Identify the parasite.
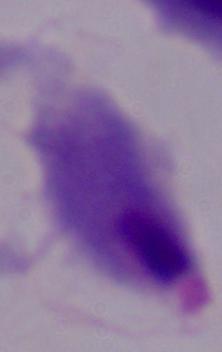
This is a trichomonad.

Summary:
  - Modality: micrograph
  - Magnification: 1000x